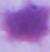

Summary:
  - Identification: erythrocyte
  - Modality: micrograph
  - Magnification: 1000x